Locate every uninfected red blood cell.
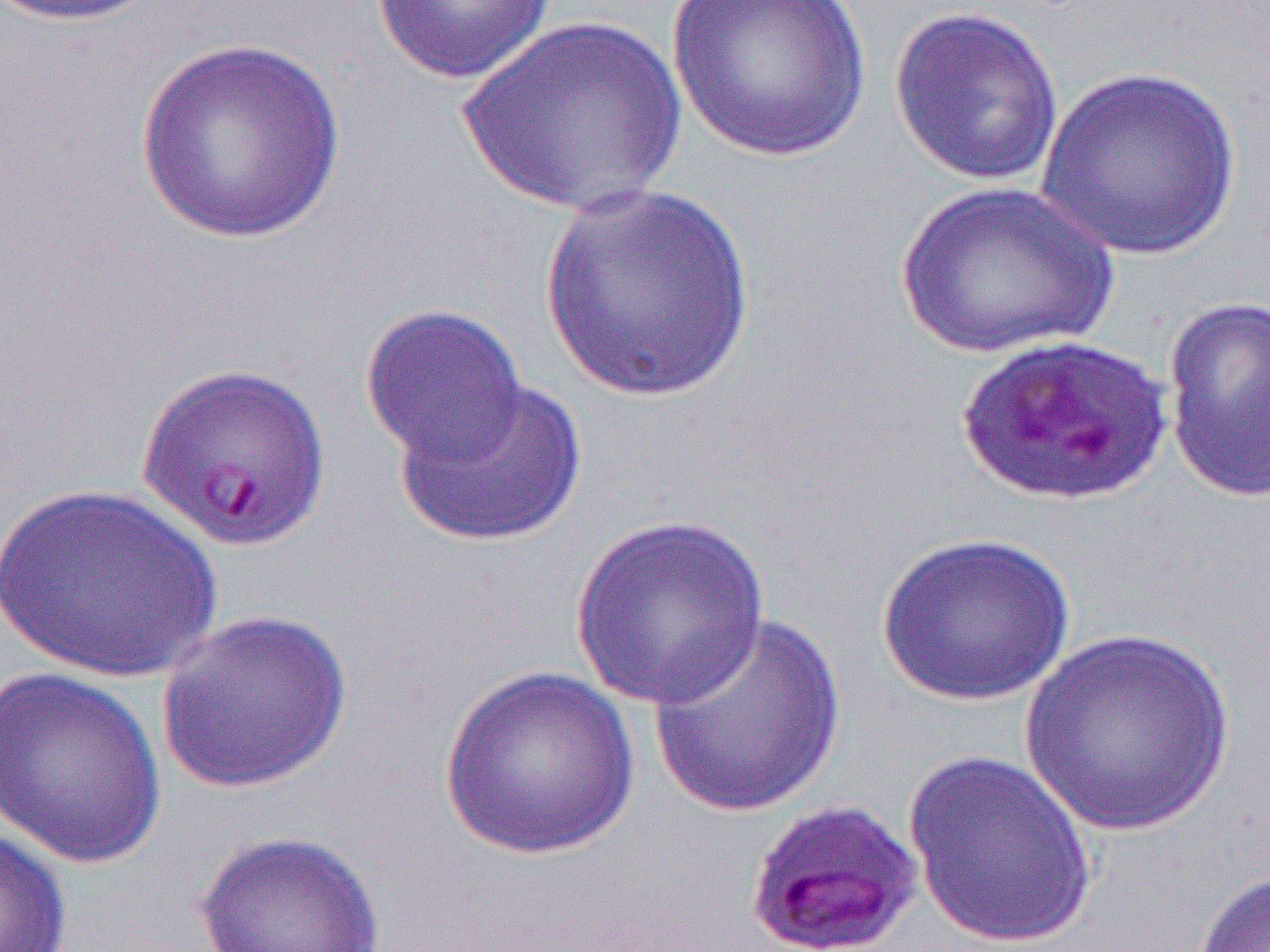

Approximate bounding boxes as (x1, y1, x2, y2) in pixels.
Uninfected red blood cells (subset): (4, 0, 170, 27), (373, 0, 558, 85), (665, 0, 874, 165), (888, 5, 1064, 188), (462, 15, 686, 220), (136, 38, 345, 244), (1033, 64, 1242, 263), (894, 180, 1118, 359), (537, 183, 757, 406), (1161, 295, 1270, 504), (359, 303, 529, 471), (392, 374, 589, 549), (1, 483, 222, 684), (570, 513, 772, 710), (876, 531, 1077, 707), (156, 609, 353, 795), (647, 613, 845, 818), (1016, 626, 1239, 838), (439, 665, 640, 860), (0, 667, 168, 869), (903, 750, 1099, 950), (0, 823, 71, 951), (193, 829, 386, 952), (1191, 865, 1270, 952).

Summary:
  - Slide-level diagnosis: Plasmodium falciparum
  - Image size: 1270×952 pixels
  - Preparation: thin blood smear
  - Modality: light microscopy
  - Magnification: 1000x
  - Field of view: one of a larger specimen